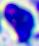

{
  "magnification": "400x",
  "modality": "micrograph",
  "identification": "white blood cell"
}